Describe the morphology of the red blood cells.
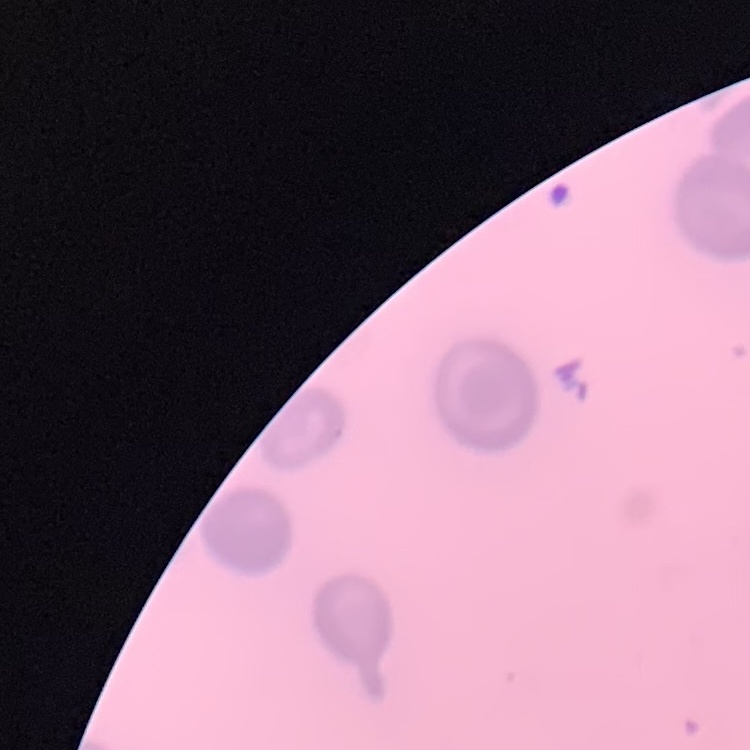

They show no rouleaux formation.

{
  "image_type": "one tile cut from a larger photomicrograph",
  "stain": "Field's or Giemsa",
  "preparation": "thin blood smear"
}